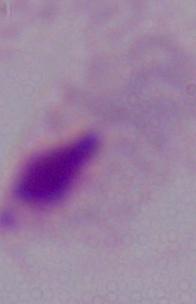 Micrograph. A trichomonad is seen. 1000x magnification.